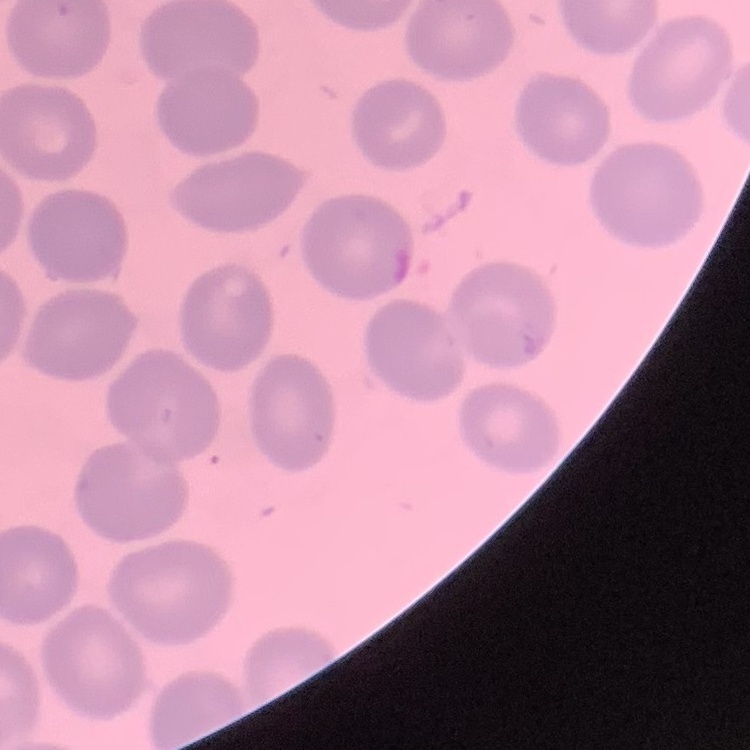

The red blood cells exhibit no rouleaux formation. One tile cut from a larger photomicrograph. Field's or Giemsa stain. Thin peripheral smear.